Comment on the morphology of the red blood cells.
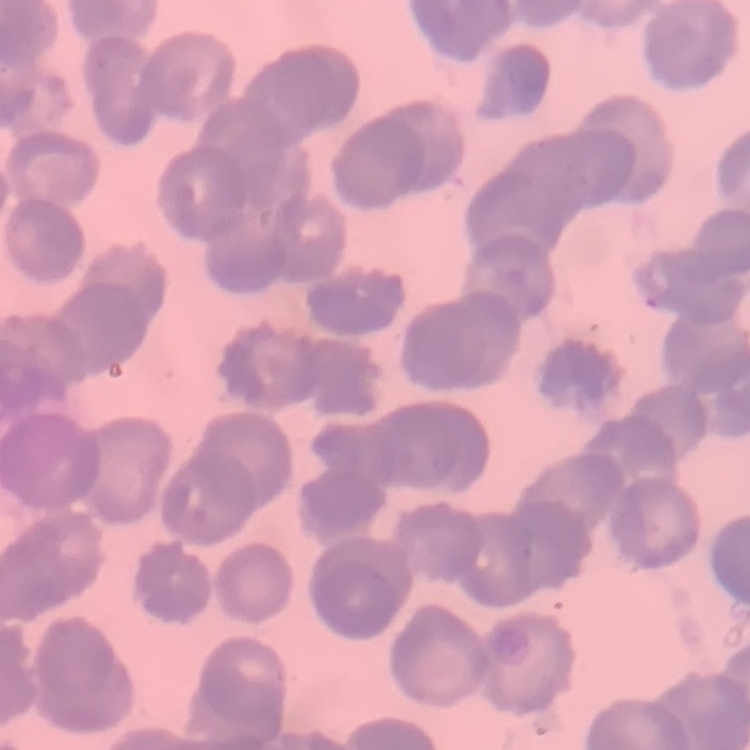

Rouleaux formation.

Square crop of a larger photomicrograph. Thin peripheral smear. Stained with either Field's or Giemsa.